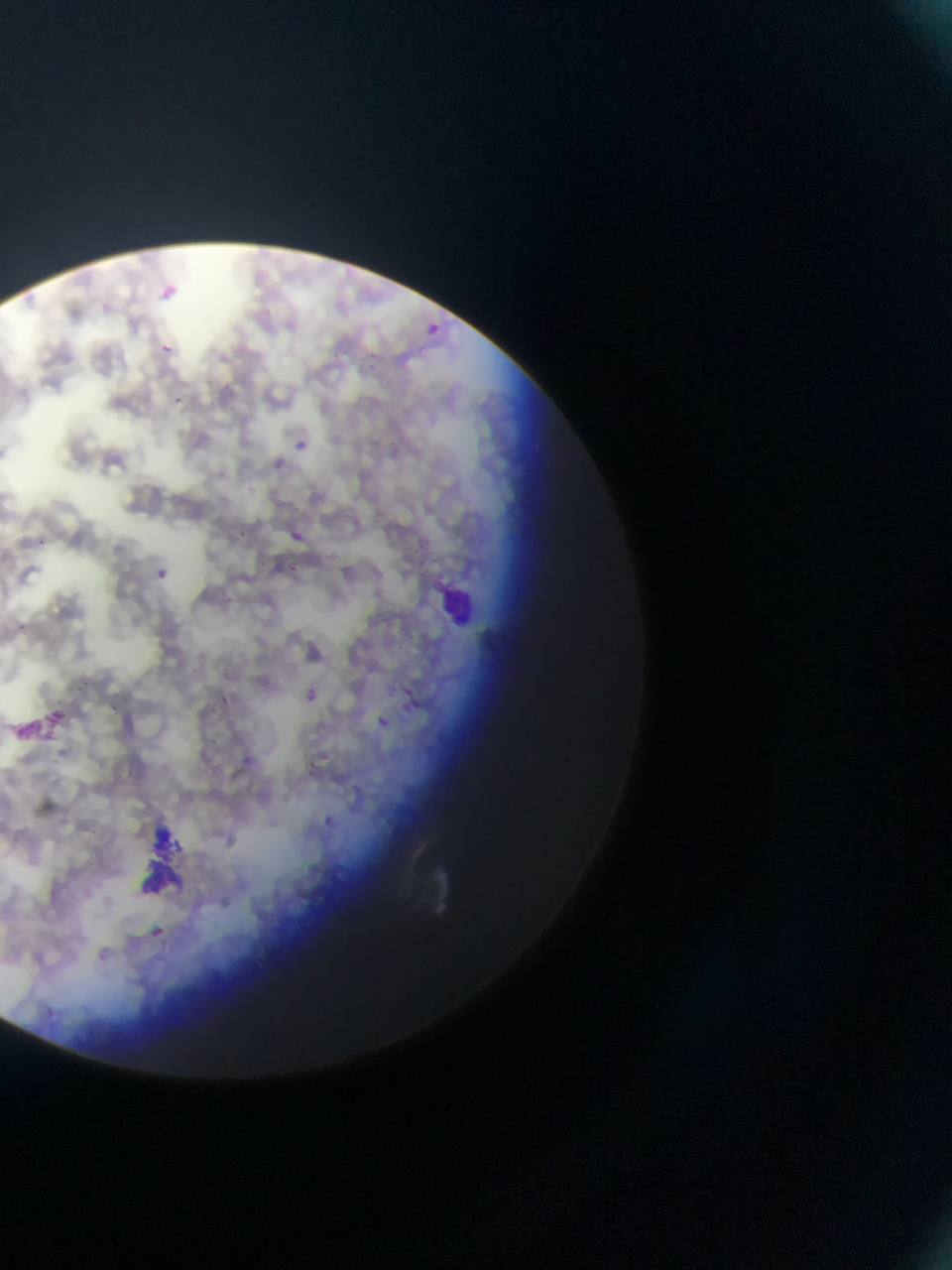
artifact (stain precipitate or debris) locations = approximate bounding boxes as [left, top, right, bottom] in pixels: [17, 703, 80, 749], [134, 820, 192, 893]
capture = mobile-phone photograph through a microscope
Plasmodium parasite locations = approximate bounding boxes as [left, top, right, bottom] in pixels: [161, 344, 173, 354], [371, 349, 383, 373], [174, 396, 189, 413], [293, 439, 304, 448], [276, 455, 293, 478], [286, 530, 302, 542], [415, 556, 434, 575], [284, 562, 303, 576], [155, 568, 175, 590], [310, 687, 322, 701], [219, 690, 236, 710], [409, 696, 423, 713], [372, 710, 390, 724], [323, 813, 342, 829], [150, 927, 166, 941]
preparation = thin blood film
country = Ghana
field of view = single
leukocyte locations = approximate bounding boxes as [left, top, right, bottom] in pixels: [427, 322, 449, 348], [440, 586, 478, 627]
image size = 952×1270 pixels